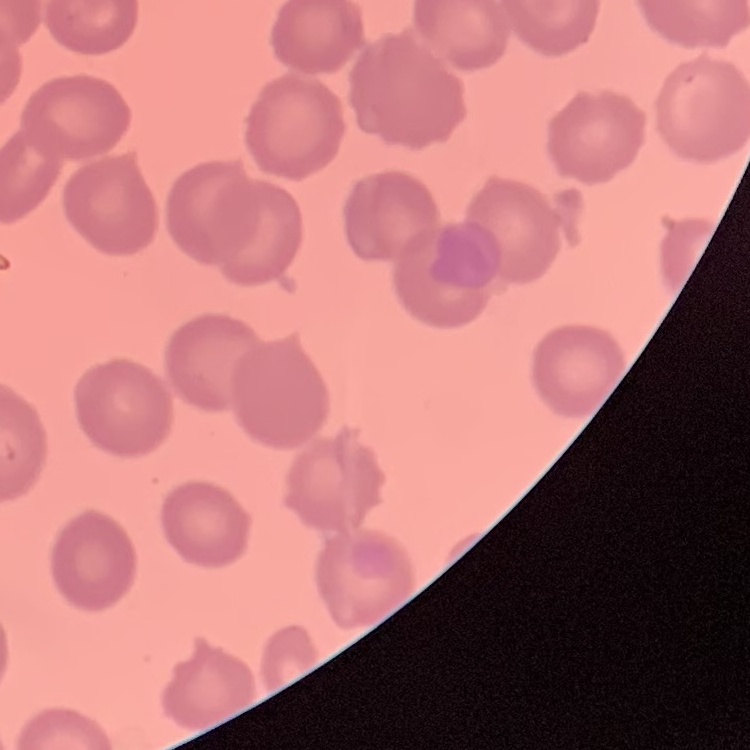

erythrocyte morphology = no rouleaux formation
image type = square crop of a larger photomicrograph
stain = Field's or Giemsa
preparation = thin peripheral smear